State which parasite is depicted.
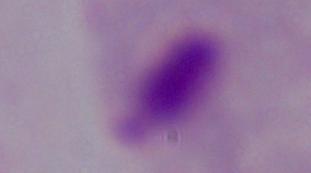

This is a trichomonad.

modality = micrograph
magnification = 1000x